Assess this cell for malaria.
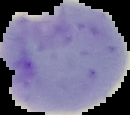

It is parasitized.

Summary:
  - Image size: 130×115 pixels
  - Image type: segmented cell region with the area outside set to black
  - Preparation: thin blood smear